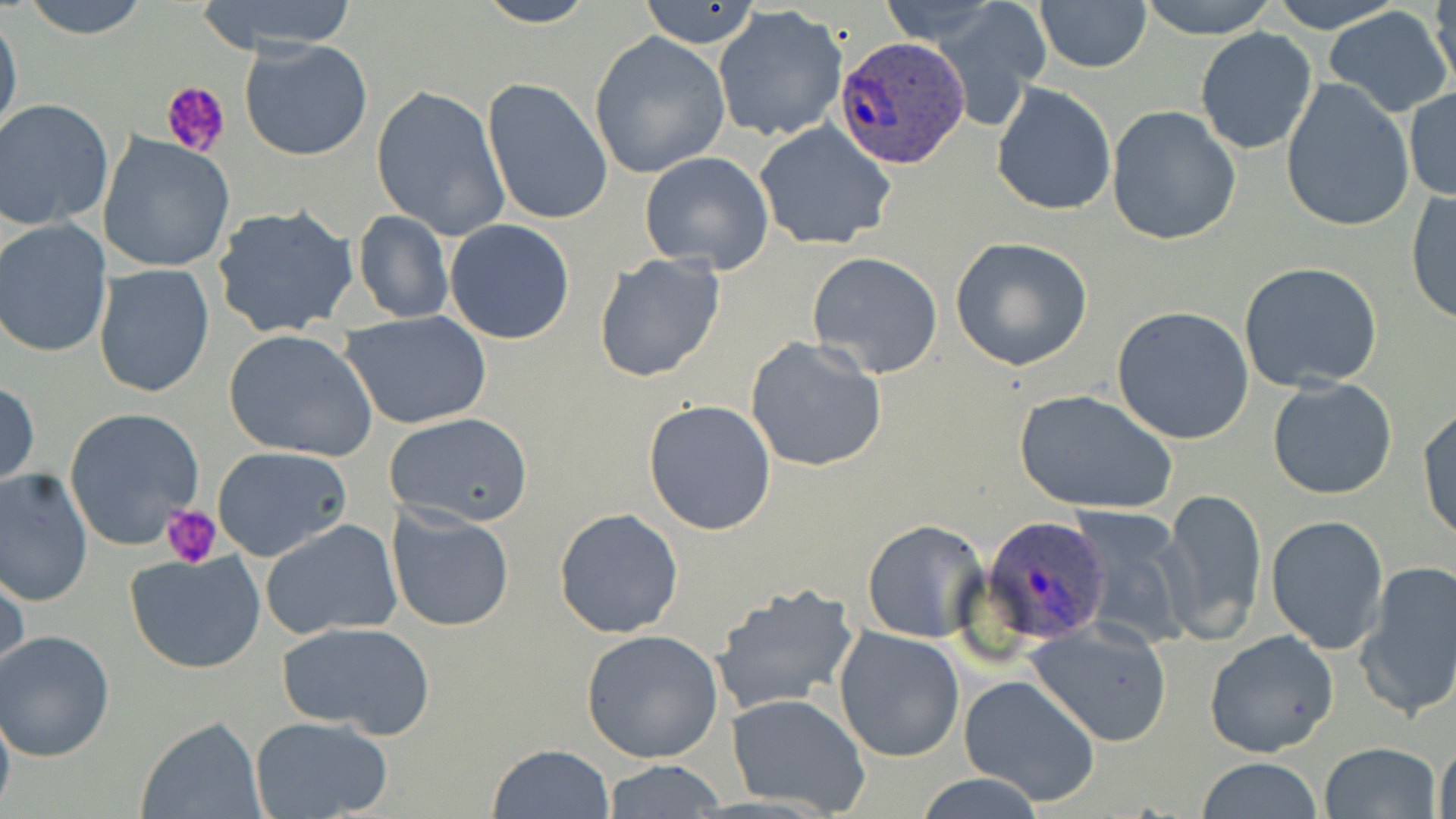
Summary:
  - Coordinate format: approximate bounding boxes as named x1/y1/x2/y2 corners in pixels
  - Platelet locations: (x1=162, y1=78, x2=231, y2=158), (x1=161, y1=504, x2=222, y2=568)
  - Uninfected red blood cell locations: (x1=19, y1=0, x2=151, y2=40), (x1=191, y1=0, x2=362, y2=56), (x1=469, y1=0, x2=602, y2=27), (x1=636, y1=0, x2=767, y2=49), (x1=1035, y1=0, x2=1151, y2=72), (x1=1137, y1=0, x2=1279, y2=40), (x1=1263, y1=0, x2=1407, y2=33), (x1=1429, y1=0, x2=1456, y2=97), (x1=877, y1=2, x2=1003, y2=45), (x1=1322, y1=5, x2=1455, y2=119), (x1=713, y1=6, x2=848, y2=141), (x1=0, y1=8, x2=22, y2=148), (x1=936, y1=9, x2=1052, y2=114), (x1=1194, y1=28, x2=1319, y2=156), (x1=589, y1=32, x2=732, y2=179), (x1=240, y1=39, x2=373, y2=162), (x1=482, y1=77, x2=612, y2=226), (x1=1280, y1=80, x2=1414, y2=233), (x1=990, y1=82, x2=1117, y2=215), (x1=371, y1=84, x2=511, y2=241), (x1=1404, y1=86, x2=1456, y2=202), (x1=0, y1=100, x2=116, y2=232), (x1=1107, y1=106, x2=1242, y2=248), (x1=755, y1=120, x2=898, y2=251), (x1=100, y1=134, x2=236, y2=275), (x1=639, y1=151, x2=774, y2=273), (x1=1405, y1=187, x2=1456, y2=328), (x1=211, y1=203, x2=362, y2=342), (x1=351, y1=210, x2=453, y2=324), (x1=1, y1=220, x2=115, y2=359), (x1=444, y1=220, x2=576, y2=345), (x1=950, y1=238, x2=1094, y2=371), (x1=593, y1=252, x2=727, y2=383), (x1=807, y1=252, x2=944, y2=378), (x1=1239, y1=262, x2=1386, y2=395), (x1=93, y1=264, x2=215, y2=399), (x1=1112, y1=305, x2=1253, y2=445), (x1=340, y1=310, x2=493, y2=430), (x1=222, y1=329, x2=378, y2=461), (x1=744, y1=335, x2=888, y2=472), (x1=1266, y1=378, x2=1398, y2=501), (x1=0, y1=379, x2=39, y2=492), (x1=1013, y1=387, x2=1180, y2=517), (x1=644, y1=399, x2=778, y2=536), (x1=1417, y1=403, x2=1456, y2=544), (x1=63, y1=407, x2=204, y2=550), (x1=384, y1=413, x2=534, y2=528), (x1=211, y1=445, x2=355, y2=564), (x1=0, y1=468, x2=95, y2=607), (x1=1158, y1=487, x2=1267, y2=644), (x1=385, y1=505, x2=515, y2=631), (x1=553, y1=507, x2=684, y2=640), (x1=1065, y1=509, x2=1195, y2=649), (x1=1265, y1=514, x2=1390, y2=655), (x1=261, y1=518, x2=402, y2=640), (x1=862, y1=519, x2=990, y2=644), (x1=123, y1=551, x2=266, y2=673), (x1=0, y1=558, x2=27, y2=685), (x1=1355, y1=560, x2=1456, y2=720), (x1=711, y1=583, x2=860, y2=718), (x1=276, y1=621, x2=436, y2=740), (x1=1027, y1=621, x2=1173, y2=746), (x1=833, y1=627, x2=967, y2=762), (x1=581, y1=629, x2=726, y2=763), (x1=1, y1=630, x2=118, y2=761), (x1=1204, y1=630, x2=1339, y2=758), (x1=957, y1=674, x2=1100, y2=807), (x1=0, y1=690, x2=17, y2=819), (x1=727, y1=692, x2=871, y2=816), (x1=249, y1=715, x2=395, y2=819), (x1=136, y1=716, x2=265, y2=819), (x1=1435, y1=737, x2=1455, y2=819), (x1=485, y1=742, x2=616, y2=818), (x1=1317, y1=742, x2=1442, y2=819), (x1=602, y1=759, x2=727, y2=817), (x1=1195, y1=759, x2=1324, y2=818), (x1=911, y1=774, x2=1051, y2=818)
  - Plasmodium ovale-infected red blood cell locations: (x1=833, y1=37, x2=971, y2=171), (x1=981, y1=514, x2=1112, y2=646)
  - Slide-level diagnosis: Plasmodium ovale
  - Field of view: one of a larger specimen
  - Magnification: 1000x
  - Modality: light microscopy
  - Stain: May-Grünwald-Giemsa
  - Preparation: thin blood smear
  - Image size: 1456×819 pixels